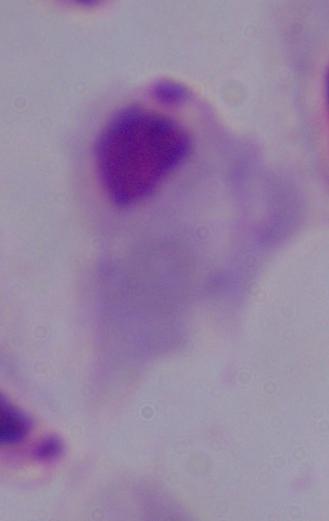 Micrograph. 1000x magnification. A trichomonad is shown.